Locate platelets.
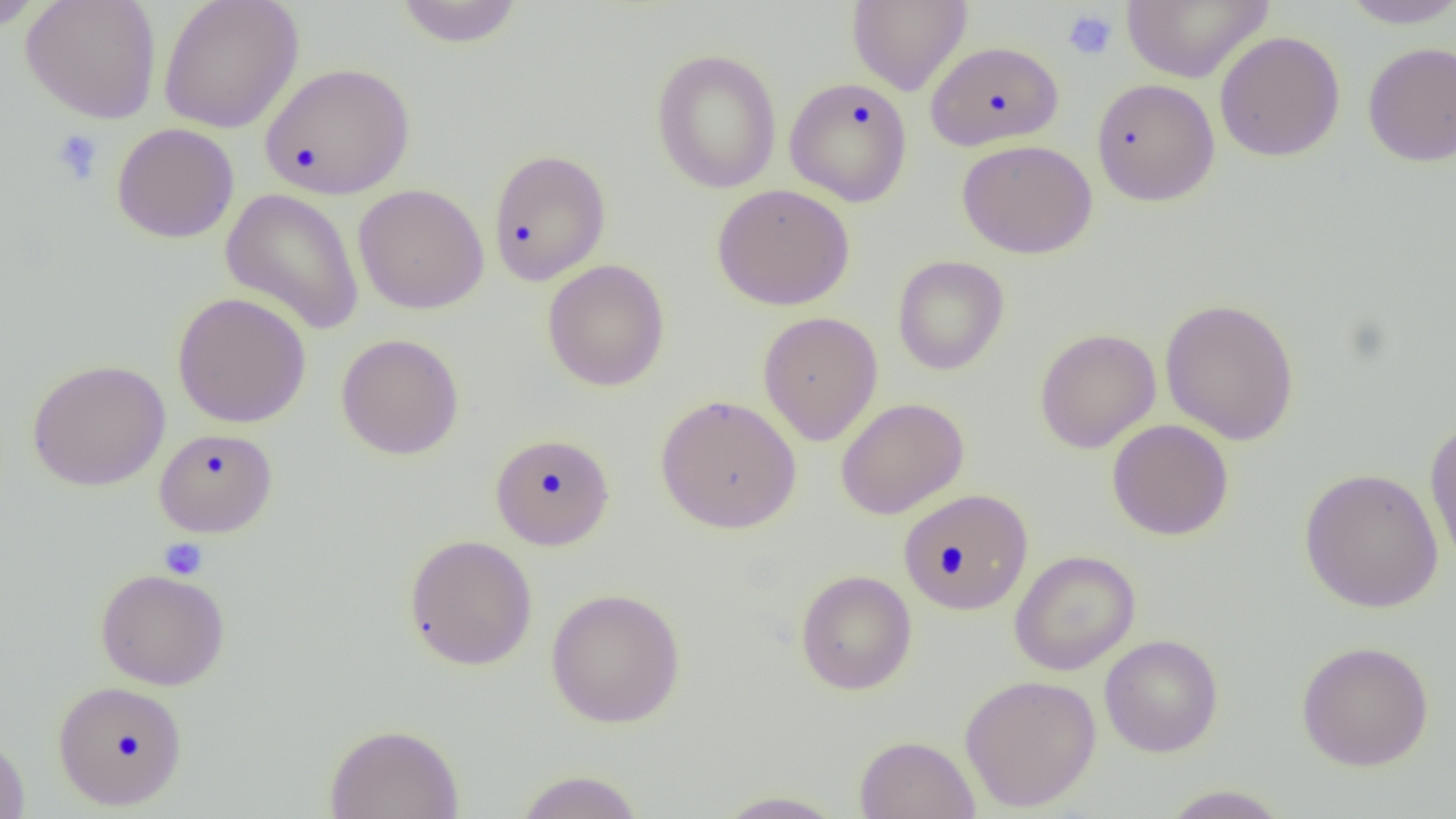
Approximate bounding boxes as (x1,y1)-(x2,y2) corner pairs in pixels.
Platelets: (1062,9)-(1118,61), (51,128)-(104,185), (159,538)-(208,580).

Uninfected red blood cell locations: (21,0)-(162,124), (158,0)-(304,134), (1121,0)-(1273,83), (1339,0)-(1456,29), (0,1)-(47,32), (393,1)-(525,48), (847,1)-(972,96), (1214,31)-(1345,162), (926,40)-(1064,150), (1362,41)-(1456,167), (651,48)-(782,194), (260,62)-(415,199), (784,76)-(913,206), (1091,78)-(1220,205), (111,122)-(240,243), (956,139)-(1097,259), (487,148)-(612,286), (353,183)-(489,314), (712,183)-(855,310), (220,188)-(365,334), (892,255)-(1009,376), (542,259)-(670,392), (172,291)-(311,428), (1160,298)-(1300,446), (758,311)-(882,445), (1034,328)-(1161,454), (336,333)-(464,460), (27,359)-(170,491), (655,393)-(802,533), (835,397)-(969,519), (1424,418)-(1456,570), (1107,419)-(1234,541), (154,427)-(277,537), (490,432)-(615,550), (1299,467)-(1444,613), (898,488)-(1034,615), (404,533)-(538,671), (1009,549)-(1141,675), (95,568)-(230,690), (795,569)-(917,695), (546,587)-(685,728), (1099,634)-(1223,757), (1295,641)-(1434,770), (959,674)-(1102,812), (52,680)-(188,810), (324,723)-(465,819), (0,731)-(30,819), (854,735)-(980,819), (513,769)-(645,818), (1159,784)-(1292,818), (713,790)-(850,818). Slide-level diagnosis: negative for blood parasites. Image is 1456×819 pixels. Thin blood smear. Optical microscopy. One field of a larger specimen. Captured at 1000x magnification.